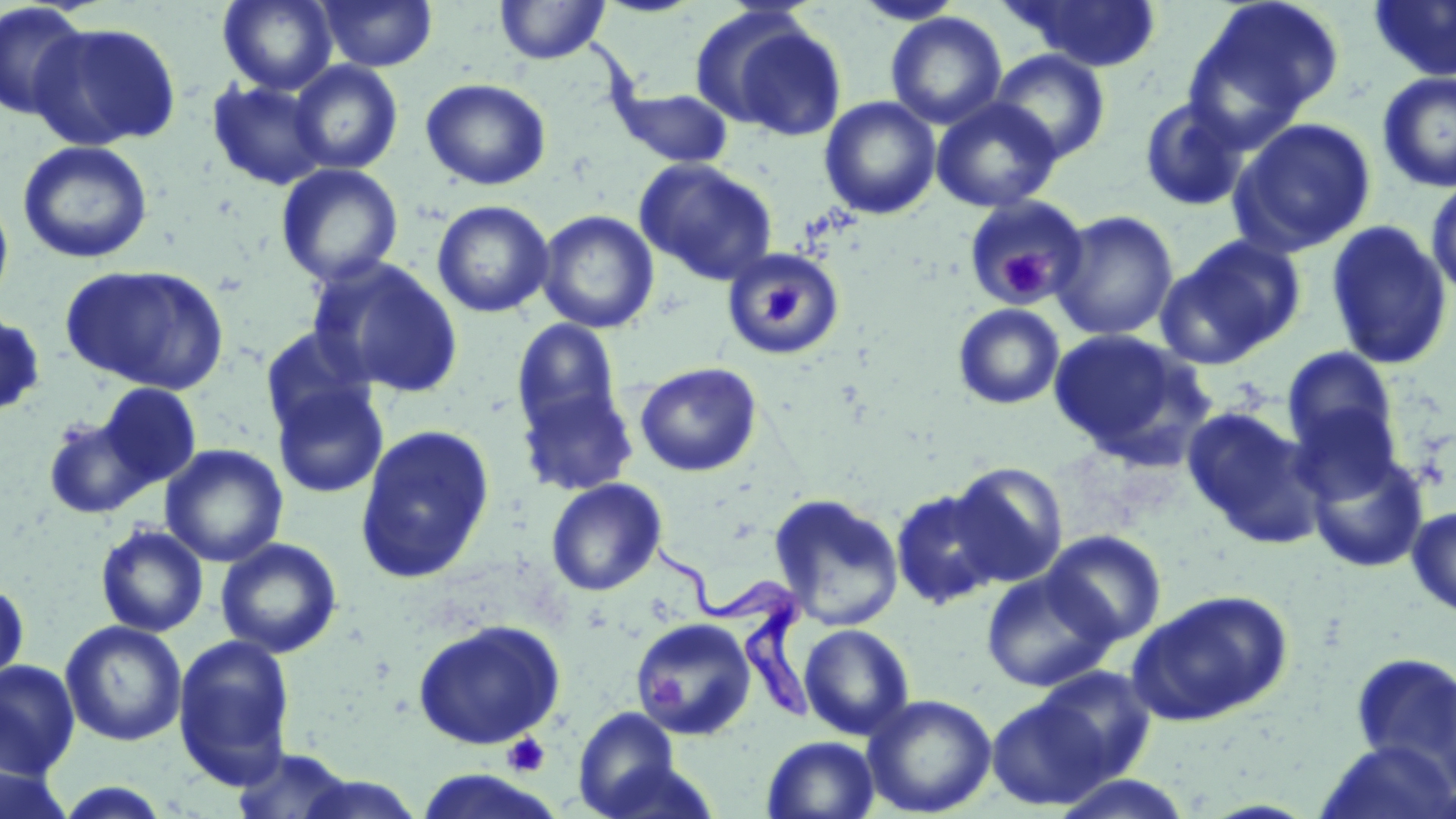

slide-level diagnosis = Trypanosoma brucei
image size = 1456×819 pixels
Trypanosoma brucei locations = approximate bounding boxes as (x1,y1)-(x2,y2) corner pairs in pixels: (651,540)-(815,723)
stain = May-Grünwald-Giemsa
magnification = 1000x
uninfected red blood cell locations = approximate bounding boxes as (x1,y1)-(x2,y2) corner pairs in pixels: (218,0)-(338,94), (317,0)-(437,71), (494,0)-(611,65), (850,0)-(968,25), (1009,0)-(1162,71), (1182,0)-(1345,141), (1367,0)-(1456,82), (0,2)-(91,122), (885,12)-(1007,130), (704,13)-(848,141), (29,21)-(182,151), (989,50)-(1111,163), (289,60)-(403,175), (1377,72)-(1456,192), (420,78)-(551,190), (206,79)-(330,191), (611,85)-(734,168), (819,96)-(941,220), (1138,96)-(1250,212), (931,98)-(1062,213), (1228,117)-(1378,256), (17,140)-(153,264), (634,158)-(779,286), (275,162)-(404,288), (1425,174)-(1456,305), (0,192)-(14,313), (964,193)-(1091,306), (431,199)-(554,318), (536,209)-(659,334), (1050,209)-(1179,341), (1325,219)-(1454,371), (1156,234)-(1306,368), (722,247)-(845,360), (307,256)-(464,398), (60,263)-(230,395), (952,303)-(1066,410), (0,308)-(46,420), (512,318)-(623,436), (259,326)-(377,437), (1047,329)-(1209,465), (1280,346)-(1401,466), (634,361)-(762,477), (271,380)-(390,500), (96,382)-(202,490), (517,383)-(638,496), (1287,404)-(1405,509), (1181,406)-(1323,547), (41,413)-(148,520), (354,424)-(495,584), (160,444)-(288,567), (1305,447)-(1430,573), (946,461)-(1069,586), (546,477)-(667,596), (889,487)-(1005,610), (769,492)-(906,631), (1406,505)-(1456,618), (95,523)-(209,637), (1042,530)-(1167,647), (215,538)-(343,658), (980,568)-(1118,692), (0,575)-(30,694), (1127,589)-(1294,726), (411,618)-(567,749), (634,618)-(757,740), (60,620)-(187,746), (799,623)-(916,741), (172,633)-(296,790), (1349,654)-(1456,782), (0,659)-(81,780), (1028,666)-(1157,788), (862,693)-(997,817), (986,693)-(1116,811), (572,707)-(687,818), (762,735)-(881,819), (1314,740)-(1456,819), (231,746)-(360,819), (1,763)-(75,819), (290,772)-(424,819), (1048,773)-(1196,818), (51,782)-(175,818)
platelet locations = approximate bounding boxes as (x1,y1)-(x2,y2) corner pairs in pixels: (996,255)-(1051,300), (765,284)-(803,321), (648,676)-(684,708), (503,733)-(550,777)
preparation = thin blood smear
field of view = single
modality = optical microscopy